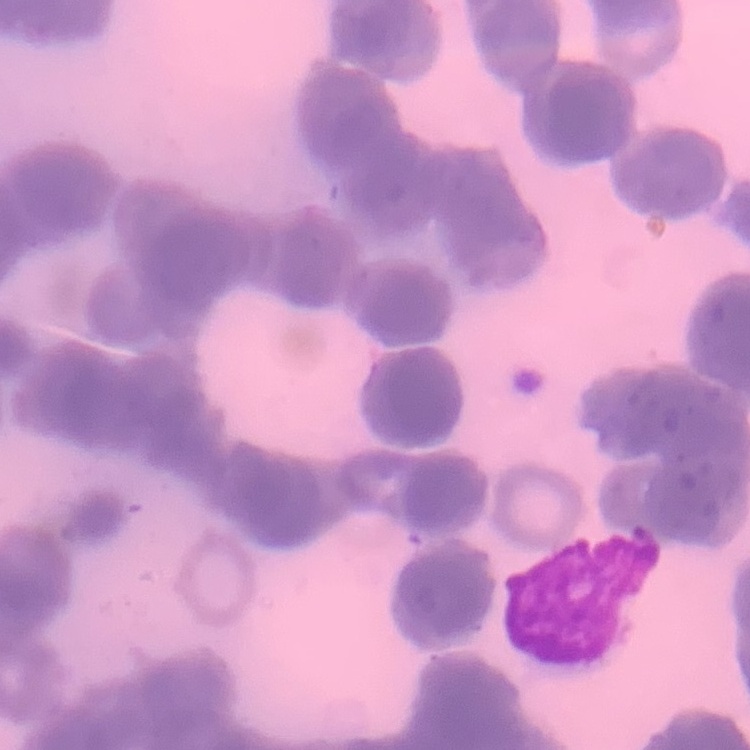
Summary:
  - Erythrocyte morphology: rouleaux formation
  - Preparation: thin peripheral smear
  - Stain: Field's or Giemsa
  - Image type: one tile cut from a larger photomicrograph